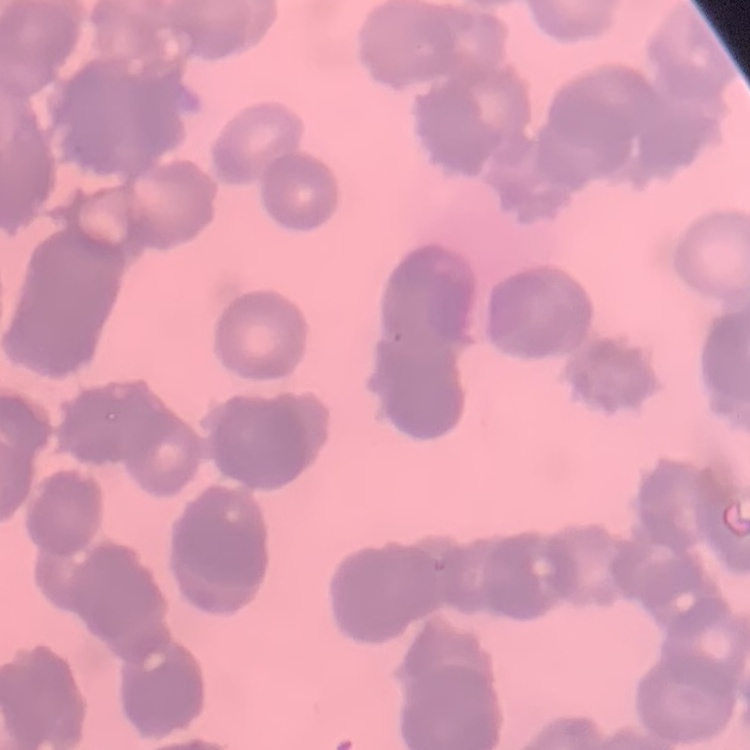
red blood cell morphology = rouleaux formation
stain = Field's or Giemsa
image type = square crop of a larger photomicrograph
preparation = thin blood smear